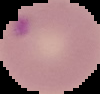
Summary:
  - Image size: 100×94 pixels
  - Image type: segmented cell region on a black background
  - Preparation: thin blood smear
  - Result: Plasmodium parasites detected